Classify this cell by malaria status.
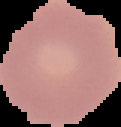

Uninfected.

Summary:
  - Preparation: thin blood smear
  - Image type: segmented cell region on a black background
  - Image size: 121×127 pixels